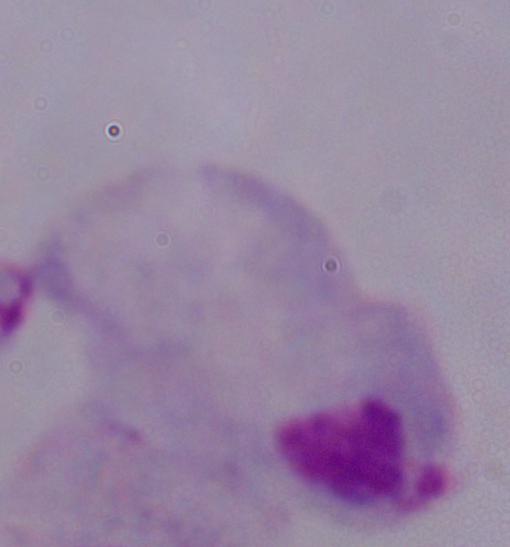
modality = micrograph
identification = trichomonad
magnification = 1000x